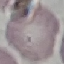
result = negative for malaria parasites
capture = smartphone through the microscope eyepiece
image type = cell patch, automatically extracted from a larger field of view and resized to 64 × 64 pixels
stain = Giemsa
preparation = thin blood film